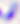
magnification = 400x
identification = Toxoplasma gondii
modality = photomicrograph